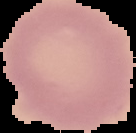
Result: no malaria parasites detected. Image is 136×133 pixels. From a thin blood smear. The area outside the segmented cell region is set to black.